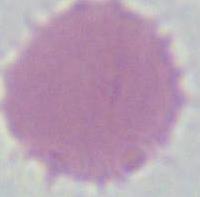

identification = red blood cell
modality = micrograph
magnification = 1000x